Locate Plasmodium malariae parasites and identify their life-cycle stages.
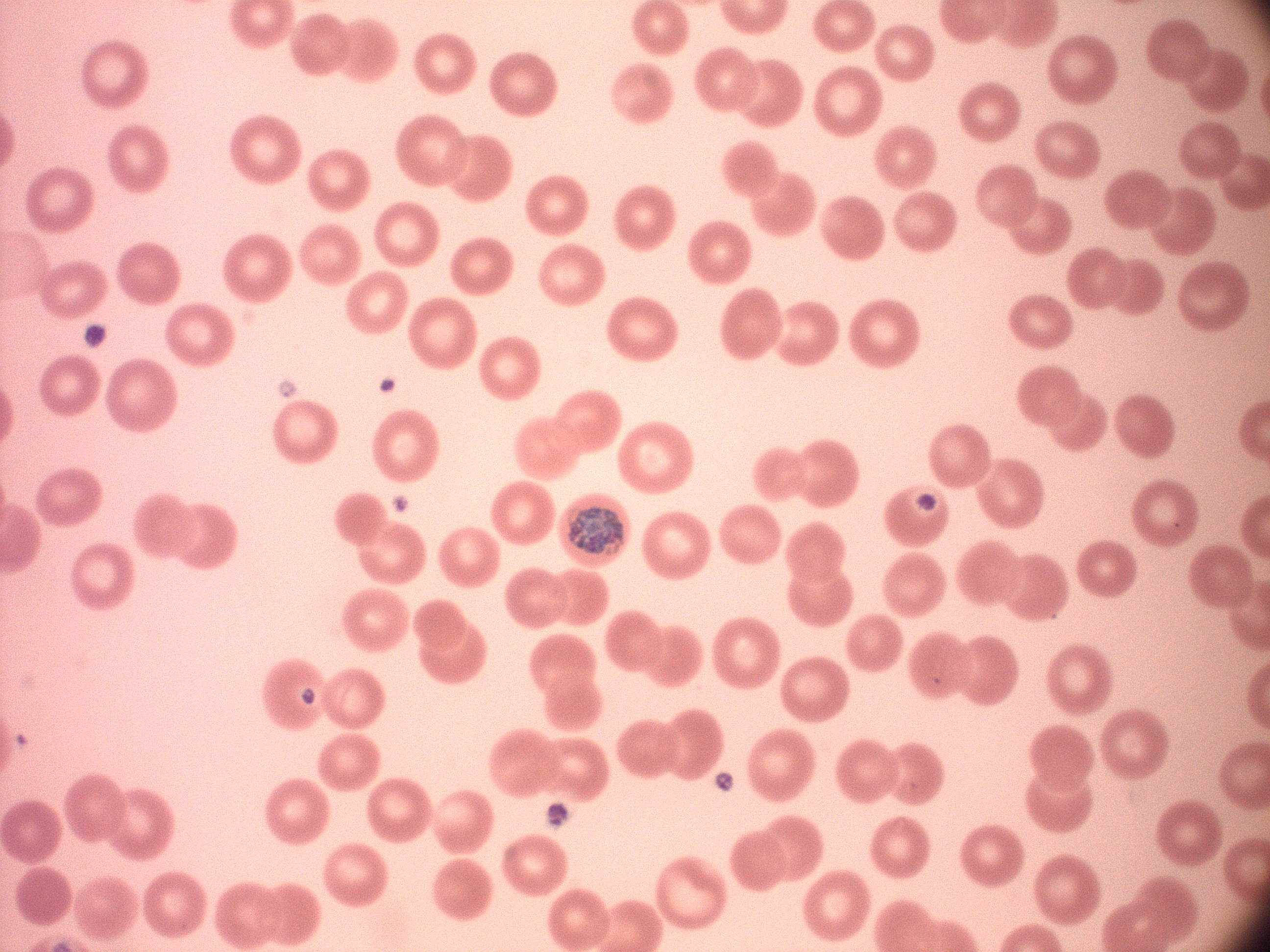

Approximate bounding boxes as (x1, y1, x2, y2) in pixels, from the source annotation, which is not necessarily exhaustive.
Schizonts: (916, 494, 938, 511), (567, 506, 624, 555).

image size = 1270×952 pixels
field of view = single
magnification = 100x
microscope = Leica DM2000 with built-in camera
species = Plasmodium malariae
preparation = thin blood smear
stain = Giemsa